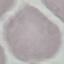
Summary:
  - Result: no malaria parasites detected
  - Stain: Giemsa
  - Preparation: thin blood film
  - Image type: automatically extracted cell patch, resized to 64 × 64 pixels
  - Capture: smartphone camera at the microscope eyepiece